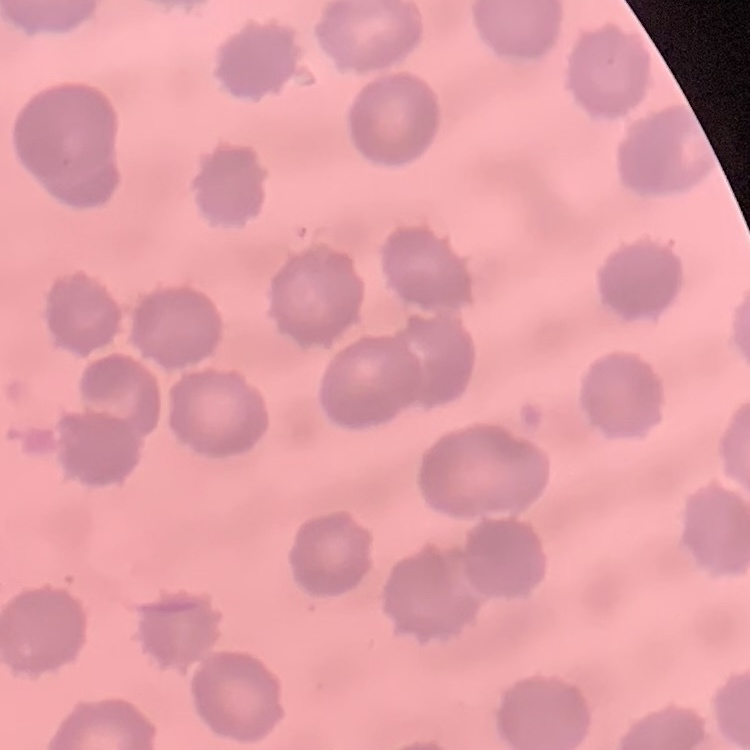
{
  "erythrocyte_morphology": "no rouleaux formation",
  "image_type": "one tile cut from a larger photomicrograph",
  "stain": "Field's or Giemsa",
  "preparation": "thin blood film"
}